Locate every leukocyte (white blood cell).
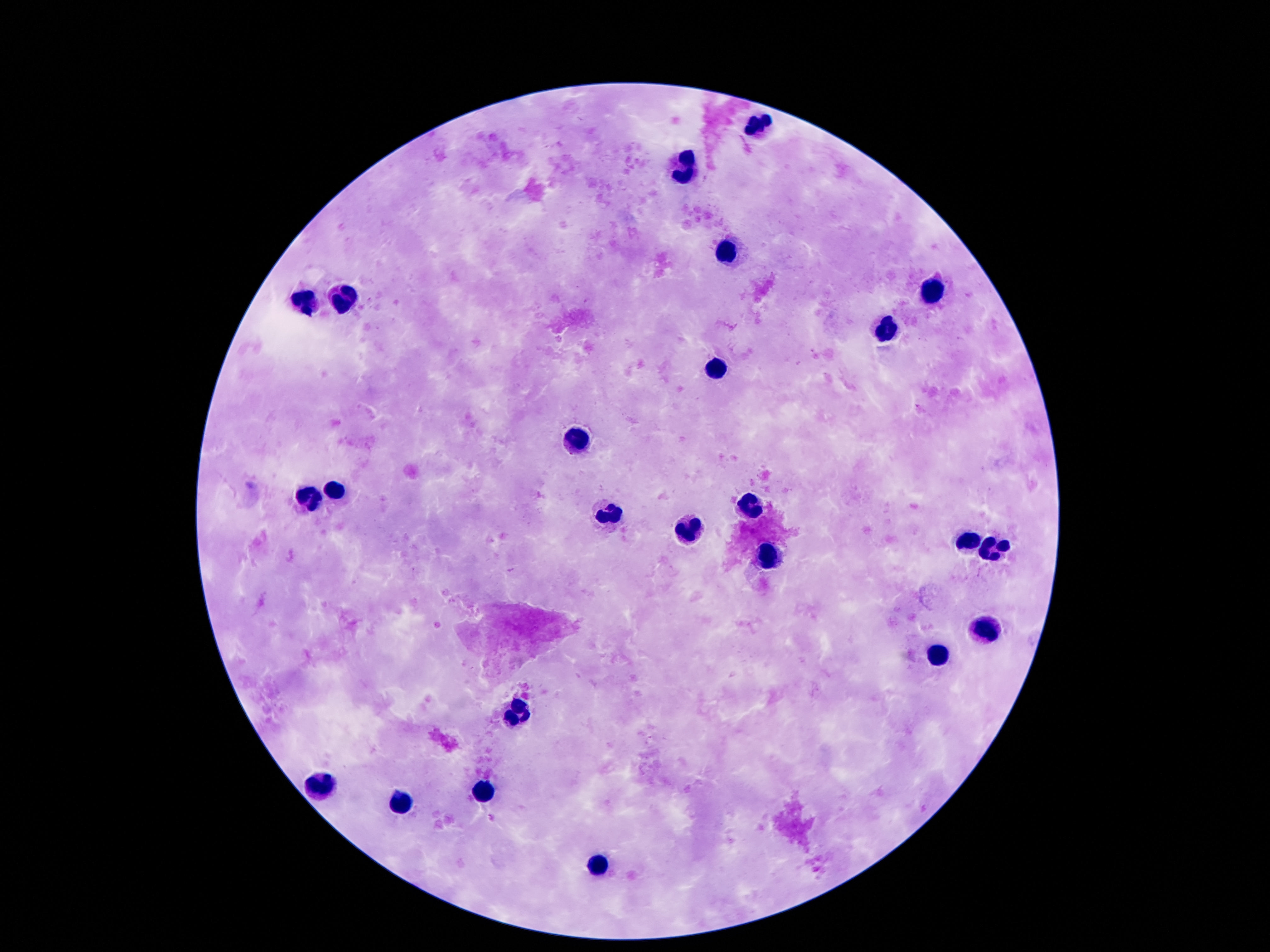
Approximate centers as (x, y) in pixels.
Leukocytes: (763, 125), (688, 172), (724, 254), (930, 289), (347, 301), (302, 302), (883, 329), (717, 368), (577, 440), (336, 488), (309, 494), (749, 506), (608, 512), (686, 531), (967, 544), (994, 551), (769, 556), (981, 630), (937, 655), (518, 712), (322, 786), (483, 791), (400, 803), (601, 868).

field of view = one from this slide
magnification = 100x
image size = 1270×952 pixels
stain = Giemsa
capture = smartphone camera through the microscope eyepiece
preparation = thick peripheral-blood smear
patient malaria status = uninfected